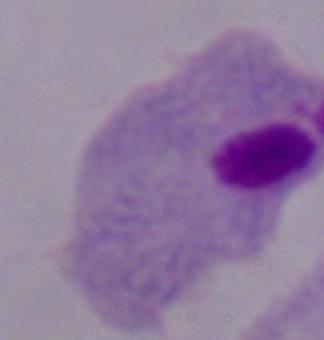
modality: micrograph
identification: trichomonad
magnification: 1000x